Classify this cell by malaria status.
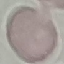
It is uninfected.

Giemsa stain. Cell patch, automatically extracted from a larger field of view and resized to 64 × 64 pixels. Photographed with a smartphone camera at the microscope eyepiece. Thin blood smear.